Give the position of every Plasmodium parasite.
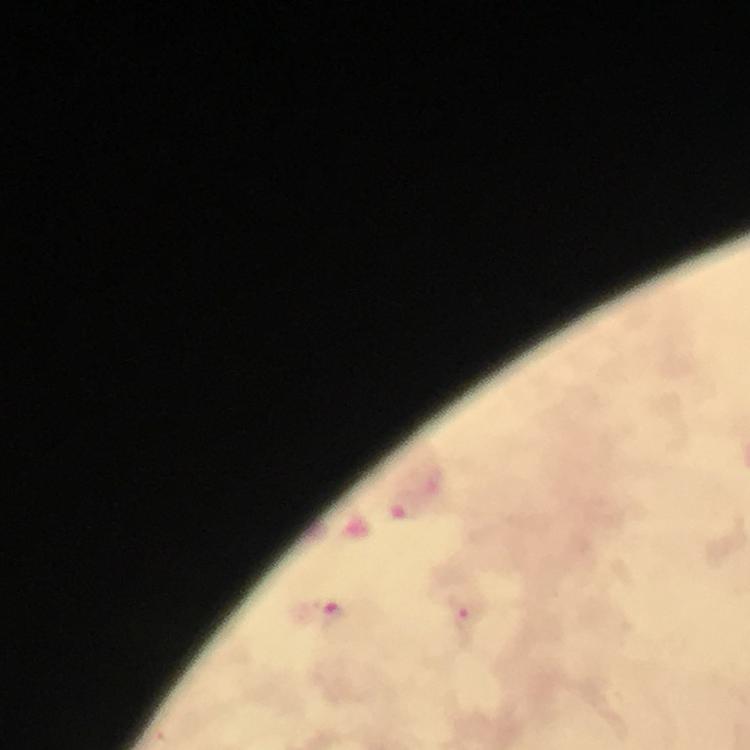

Approximate object centers, in pixels from the top-left corner.
Plasmodium parasites: (x=405, y=505), (x=332, y=616), (x=463, y=617).

A crop from one field of view. Giemsa stain. Image is 750×750 pixels. From a malaria diagnostic workup. At 100x magnification. Immersion oil applied. Thick blood film. Photographed through the microscope with a smartphone camera.